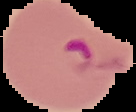

Summary:
  - Preparation: thin blood film
  - Image size: 136×112 pixels
  - Result: malaria parasites detected
  - Image type: segmented cell region with the area outside set to black